Outline each uninfected red blood cell.
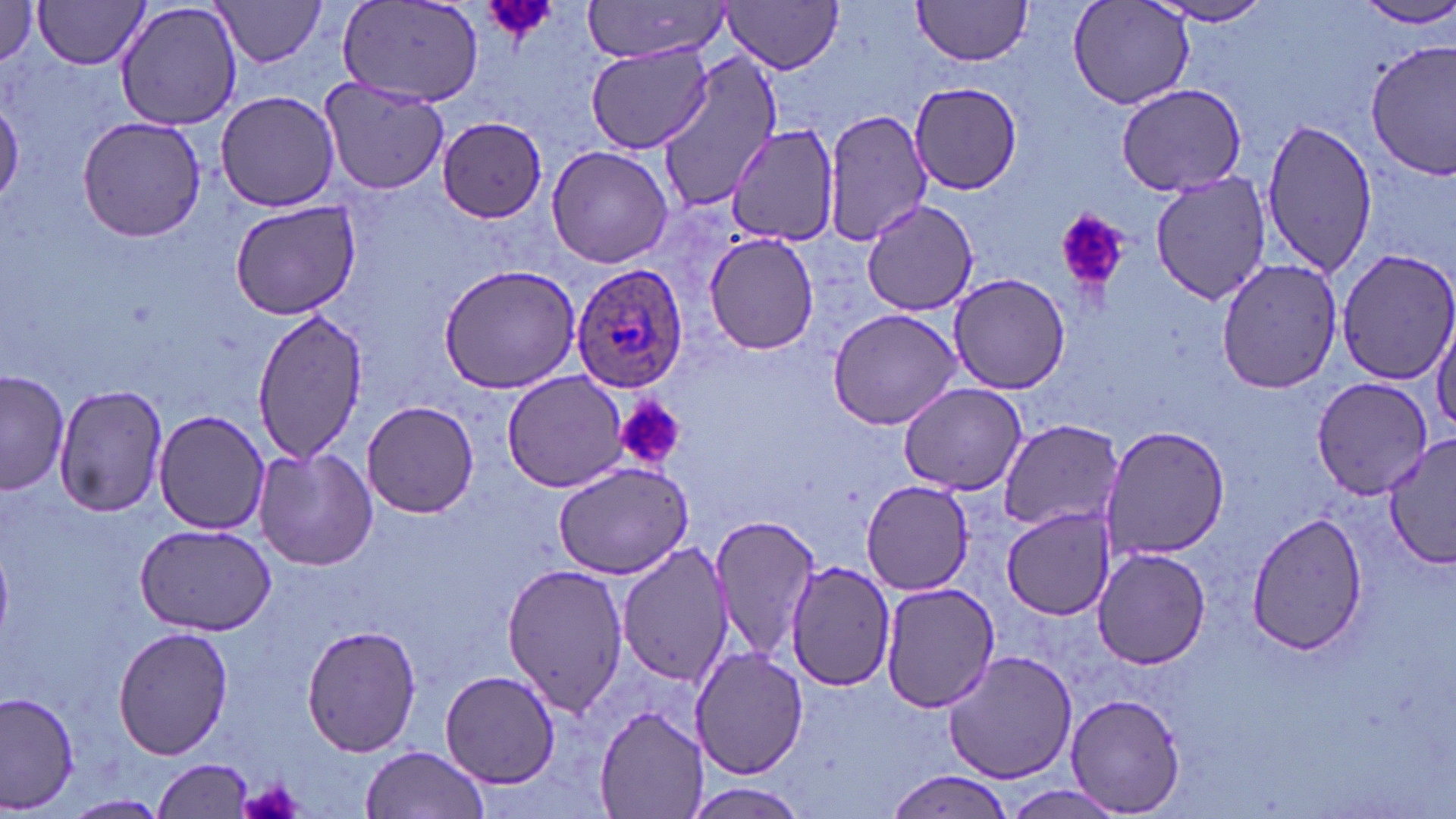

Approximate bounding boxes as named x1/y1/x2/y2 corners in pixels.
Uninfected red blood cells: (x1=33, y1=0, x2=152, y2=71), (x1=210, y1=0, x2=330, y2=68), (x1=581, y1=0, x2=735, y2=60), (x1=912, y1=0, x2=1034, y2=66), (x1=1067, y1=0, x2=1196, y2=111), (x1=1149, y1=0, x2=1278, y2=27), (x1=0, y1=1, x2=39, y2=64), (x1=114, y1=1, x2=242, y2=131), (x1=725, y1=1, x2=846, y2=73), (x1=336, y1=2, x2=486, y2=105), (x1=1355, y1=2, x2=1456, y2=29), (x1=1365, y1=39, x2=1455, y2=178), (x1=584, y1=43, x2=715, y2=155), (x1=654, y1=52, x2=786, y2=214), (x1=319, y1=77, x2=450, y2=196), (x1=908, y1=82, x2=1026, y2=196), (x1=1116, y1=84, x2=1252, y2=198), (x1=214, y1=91, x2=342, y2=211), (x1=0, y1=95, x2=23, y2=207), (x1=824, y1=108, x2=934, y2=248), (x1=77, y1=115, x2=209, y2=243), (x1=436, y1=116, x2=548, y2=221), (x1=1262, y1=117, x2=1379, y2=278), (x1=727, y1=124, x2=843, y2=244), (x1=545, y1=143, x2=677, y2=268), (x1=1150, y1=172, x2=1272, y2=304), (x1=861, y1=198, x2=981, y2=315), (x1=229, y1=202, x2=361, y2=319), (x1=703, y1=233, x2=820, y2=354), (x1=1335, y1=247, x2=1456, y2=386), (x1=1214, y1=258, x2=1345, y2=394), (x1=437, y1=264, x2=586, y2=394), (x1=949, y1=271, x2=1069, y2=394), (x1=255, y1=308, x2=369, y2=461), (x1=828, y1=308, x2=965, y2=430), (x1=1432, y1=317, x2=1456, y2=437), (x1=1, y1=371, x2=70, y2=496), (x1=502, y1=371, x2=633, y2=494), (x1=1311, y1=375, x2=1434, y2=498), (x1=898, y1=380, x2=1027, y2=495), (x1=54, y1=382, x2=169, y2=518), (x1=361, y1=400, x2=481, y2=517), (x1=154, y1=411, x2=269, y2=534), (x1=997, y1=422, x2=1124, y2=532), (x1=1100, y1=425, x2=1230, y2=558), (x1=1383, y1=435, x2=1456, y2=572), (x1=253, y1=447, x2=377, y2=571), (x1=553, y1=460, x2=697, y2=581), (x1=861, y1=481, x2=975, y2=597), (x1=1000, y1=508, x2=1118, y2=619), (x1=1247, y1=512, x2=1370, y2=653), (x1=708, y1=513, x2=821, y2=663), (x1=135, y1=522, x2=275, y2=636), (x1=616, y1=539, x2=735, y2=688), (x1=1092, y1=545, x2=1210, y2=670), (x1=785, y1=560, x2=899, y2=691), (x1=499, y1=561, x2=630, y2=715), (x1=879, y1=581, x2=999, y2=713), (x1=302, y1=625, x2=423, y2=757), (x1=113, y1=626, x2=233, y2=759), (x1=691, y1=647, x2=808, y2=779), (x1=943, y1=649, x2=1077, y2=784), (x1=441, y1=668, x2=560, y2=788), (x1=2, y1=691, x2=79, y2=812), (x1=1064, y1=691, x2=1187, y2=815), (x1=596, y1=706, x2=706, y2=818), (x1=360, y1=745, x2=491, y2=819), (x1=154, y1=758, x2=256, y2=817), (x1=886, y1=769, x2=1019, y2=817), (x1=679, y1=780, x2=812, y2=819), (x1=1005, y1=785, x2=1129, y2=817), (x1=62, y1=793, x2=172, y2=818).

Summary:
  - Platelet locations: (x1=478, y1=0, x2=560, y2=43), (x1=1055, y1=208, x2=1130, y2=294), (x1=615, y1=395, x2=685, y2=473), (x1=236, y1=779, x2=307, y2=819)
  - Plasmodium ovale-infected red blood cell locations: (x1=571, y1=263, x2=690, y2=392)
  - Slide-level diagnosis: Plasmodium ovale
  - Modality: optical microscopy
  - Stain: May-Grünwald-Giemsa
  - Image size: 1456×819 pixels
  - Field of view: one of a larger specimen
  - Magnification: 1000x
  - Preparation: thin blood smear